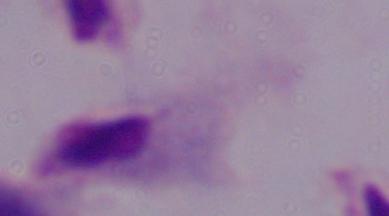

identification = trichomonad
modality = photomicrograph
magnification = 1000x